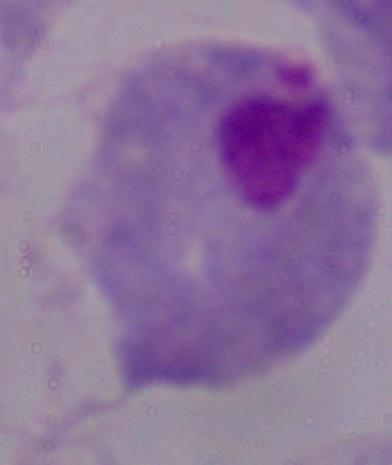

Micrograph. A trichomonad is seen. 1000x magnification.